Locate every Plasmodium falciparum-infected red blood cell.
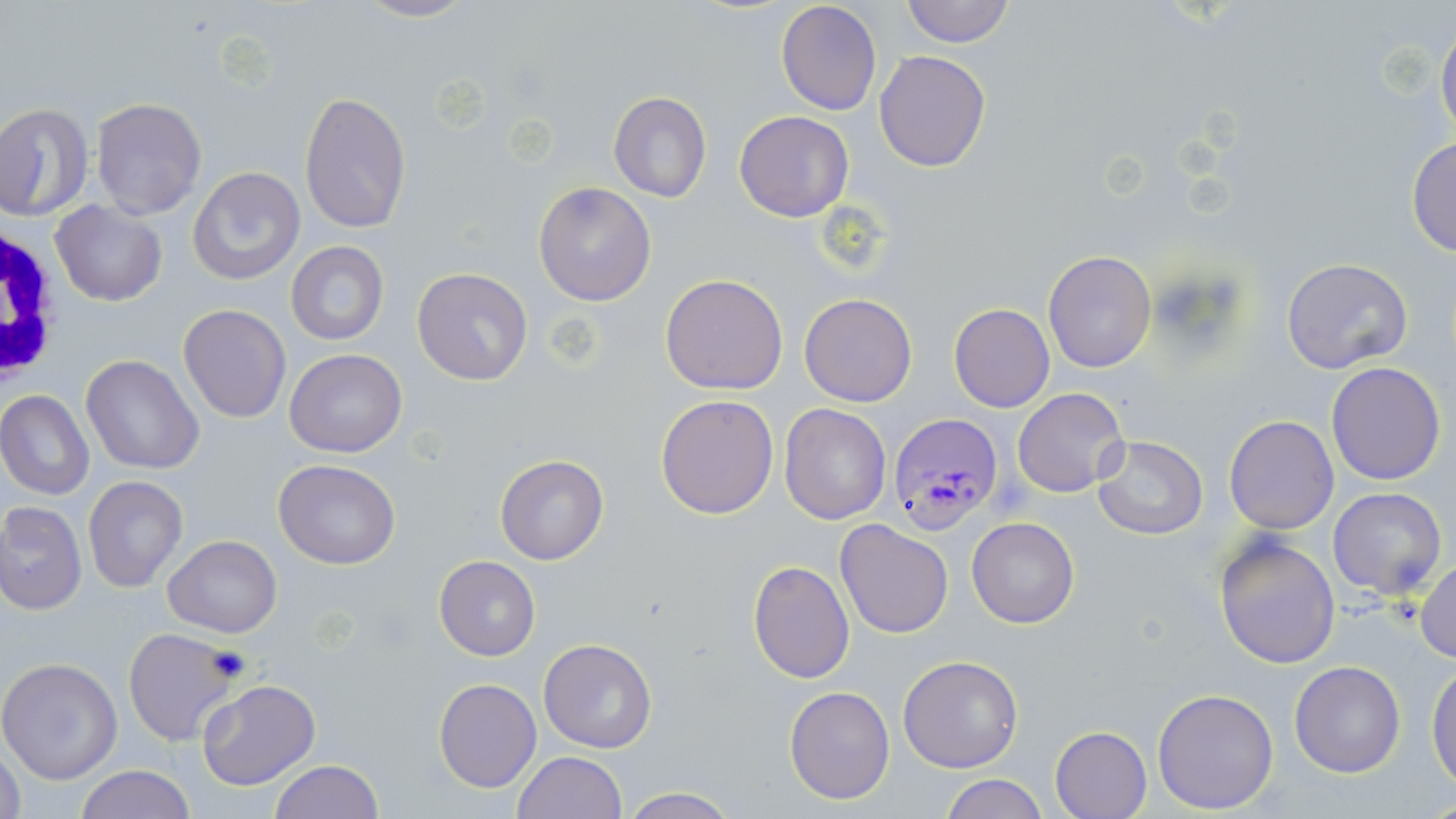

Approximate bounding boxes as [x1, y1, x2, y2] in pixels.
Plasmodium falciparum-infected red blood cells: [888, 412, 1003, 537].

Summary:
  - Uninfected red blood cell locations: [351, 0, 478, 24], [900, 0, 1015, 48], [775, 2, 882, 116], [1435, 20, 1456, 141], [875, 49, 991, 171], [299, 91, 412, 233], [608, 93, 712, 203], [92, 97, 207, 219], [0, 102, 93, 221], [734, 111, 854, 223], [1406, 138, 1456, 257], [188, 166, 306, 288], [532, 181, 656, 304], [50, 199, 167, 306], [285, 241, 388, 346], [1043, 250, 1156, 372], [1280, 256, 1413, 374], [411, 267, 533, 386], [659, 274, 788, 394], [798, 293, 919, 407], [949, 303, 1055, 412], [179, 304, 292, 422], [285, 349, 408, 458], [81, 354, 204, 475], [1326, 361, 1446, 486], [1011, 388, 1128, 496], [0, 390, 93, 500], [656, 394, 781, 520], [779, 403, 891, 525], [1224, 415, 1339, 534], [1093, 435, 1207, 540], [496, 455, 607, 565], [273, 459, 401, 568], [82, 476, 187, 592], [1328, 488, 1447, 599], [1, 501, 86, 613], [967, 517, 1079, 629], [835, 519, 954, 639], [1213, 533, 1341, 668], [163, 535, 282, 638], [434, 556, 540, 660], [748, 559, 856, 684], [1413, 559, 1456, 662], [123, 628, 243, 749], [537, 639, 658, 753], [897, 655, 1022, 773], [0, 657, 124, 784], [1288, 660, 1405, 778], [1427, 665, 1456, 788], [434, 678, 541, 792], [196, 679, 320, 789], [784, 684, 895, 804], [1152, 687, 1279, 813], [1049, 725, 1152, 819], [0, 745, 26, 819], [512, 750, 627, 818], [269, 759, 383, 818], [73, 765, 197, 819], [939, 775, 1050, 819], [617, 785, 741, 818]
  - White blood cell locations: [0, 204, 70, 396]
  - Slide-level diagnosis: Plasmodium falciparum
  - Field of view: single
  - Image size: 1456×819 pixels
  - Stain: May-Grünwald-Giemsa
  - Modality: light microscopy
  - Magnification: 1000x
  - Preparation: thin blood smear